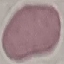
Summary:
  - Malaria status: uninfected
  - Image type: automatically extracted cell patch, resized to 64 × 64 pixels
  - Stain: Giemsa
  - Capture: smartphone through the microscope eyepiece
  - Preparation: thin blood smear